Name the blood parasite species.
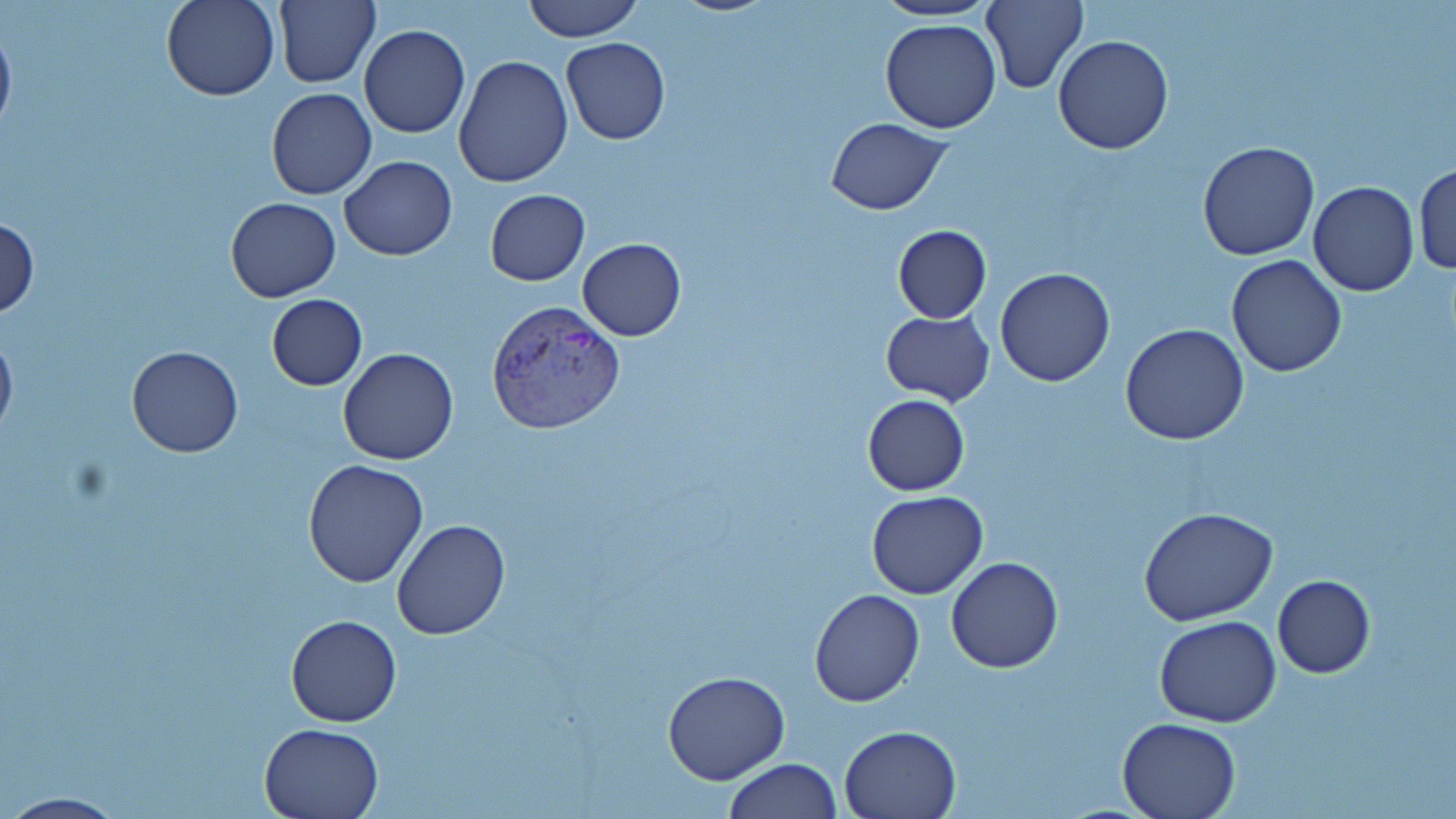
Plasmodium vivax.

Approximate bounding boxes as named x1/y1/x2/y2 corners in pixels. Plasmodium vivax-infected red blood cell locations: (x1=485, y1=298, x2=626, y2=435). Uninfected red blood cell locations: (x1=161, y1=0, x2=280, y2=101), (x1=270, y1=0, x2=380, y2=87), (x1=520, y1=0, x2=645, y2=42), (x1=666, y1=0, x2=780, y2=16), (x1=981, y1=0, x2=1087, y2=92), (x1=872, y1=2, x2=1003, y2=23), (x1=0, y1=16, x2=17, y2=144), (x1=880, y1=20, x2=1002, y2=134), (x1=359, y1=24, x2=470, y2=138), (x1=1052, y1=34, x2=1176, y2=154), (x1=560, y1=37, x2=669, y2=144), (x1=454, y1=56, x2=573, y2=188), (x1=266, y1=88, x2=377, y2=200), (x1=827, y1=118, x2=952, y2=215), (x1=1197, y1=140, x2=1321, y2=260), (x1=338, y1=155, x2=457, y2=259), (x1=1414, y1=163, x2=1456, y2=276), (x1=1308, y1=181, x2=1419, y2=297), (x1=484, y1=189, x2=589, y2=286), (x1=226, y1=197, x2=341, y2=301), (x1=0, y1=216, x2=40, y2=319), (x1=891, y1=225, x2=992, y2=324), (x1=577, y1=238, x2=686, y2=340), (x1=1225, y1=254, x2=1347, y2=376), (x1=995, y1=267, x2=1116, y2=387), (x1=265, y1=293, x2=367, y2=390), (x1=882, y1=311, x2=995, y2=405), (x1=1121, y1=322, x2=1250, y2=445), (x1=0, y1=328, x2=17, y2=446), (x1=127, y1=347, x2=243, y2=458), (x1=336, y1=349, x2=459, y2=466), (x1=862, y1=394, x2=969, y2=495), (x1=302, y1=458, x2=430, y2=589), (x1=866, y1=491, x2=989, y2=600), (x1=1138, y1=507, x2=1279, y2=625), (x1=391, y1=519, x2=510, y2=640), (x1=946, y1=556, x2=1065, y2=673), (x1=1272, y1=575, x2=1375, y2=677), (x1=809, y1=589, x2=925, y2=707), (x1=286, y1=613, x2=401, y2=727), (x1=1155, y1=616, x2=1282, y2=728), (x1=661, y1=671, x2=790, y2=786), (x1=1117, y1=717, x2=1240, y2=818), (x1=258, y1=721, x2=385, y2=818), (x1=839, y1=724, x2=961, y2=818), (x1=723, y1=758, x2=841, y2=819), (x1=0, y1=793, x2=135, y2=819). 1000x magnification. Optical microscopy. Image is 1456×819 pixels. Single field of view. Thin blood smear. May-Grünwald-Giemsa stain.